Classify this cell by malaria status.
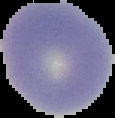
Uninfected.

Summary:
  - Image size: 115×118 pixels
  - Image type: segmented cell region on a black background
  - Preparation: thin blood smear